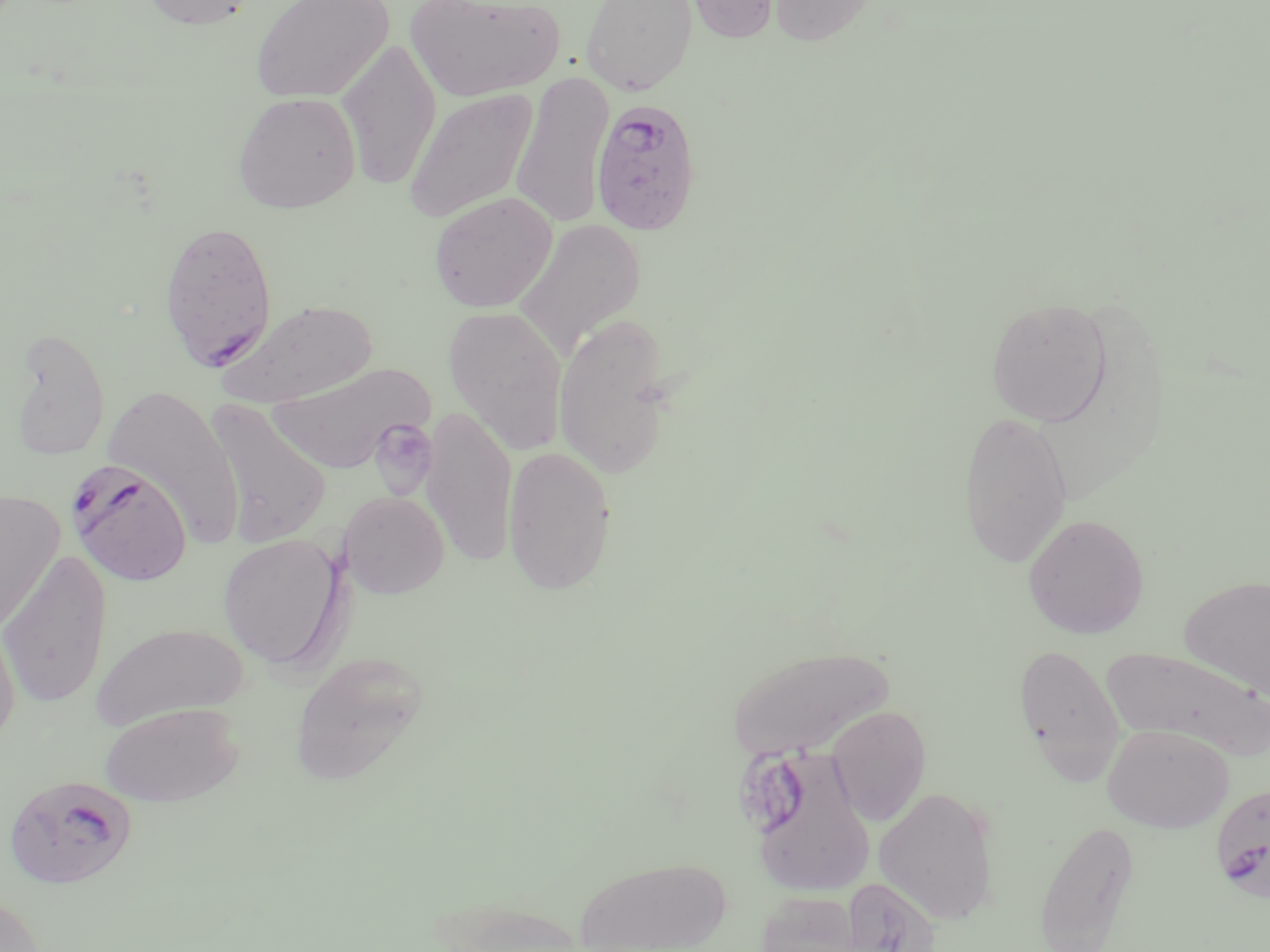

slide-level diagnosis = Plasmodium falciparum
modality = light microscopy
stain = May-Grünwald-Giemsa
field of view = one of a larger specimen
preparation = thin blood film
platelet locations = approximate bounding boxes as (x1, y1, x2, y2) in pixels: (369, 419, 437, 495)
image size = 1270×952 pixels
magnification = 1000x
Plasmodium falciparum-infected red blood cell locations = approximate bounding boxes as (x1, y1, x2, y2) in pixels: (590, 97, 703, 235), (159, 219, 278, 370), (66, 462, 192, 588), (3, 775, 138, 891), (1210, 781, 1270, 901)
uninfected red blood cell locations = approximate bounding boxes as (x1, y1, x2, y2) in pixels: (138, 0, 258, 31), (250, 0, 394, 104), (406, 0, 564, 101), (580, 0, 698, 95), (680, 0, 784, 43), (768, 0, 879, 47), (337, 37, 441, 191), (511, 71, 614, 230), (404, 88, 539, 223), (233, 91, 361, 213), (429, 192, 557, 313), (513, 219, 646, 359), (986, 298, 1112, 427), (219, 299, 378, 407), (443, 306, 568, 454), (554, 312, 676, 480), (8, 327, 111, 461), (266, 364, 431, 472), (103, 384, 244, 545), (202, 398, 332, 548), (422, 404, 518, 567), (957, 410, 1073, 568), (503, 445, 617, 593), (0, 490, 64, 634), (339, 490, 449, 598), (1023, 514, 1149, 639), (219, 534, 346, 669), (0, 550, 113, 710), (1180, 575, 1270, 701), (0, 616, 21, 749), (91, 623, 250, 730), (1012, 642, 1126, 784), (728, 645, 894, 760), (1100, 646, 1270, 761), (289, 651, 429, 786), (99, 702, 244, 807), (826, 706, 932, 825), (1103, 724, 1234, 833), (742, 747, 876, 896), (874, 786, 1000, 924), (1033, 820, 1140, 952), (575, 856, 731, 952), (838, 877, 941, 952), (755, 890, 869, 951), (0, 891, 48, 952)